Outline each blood parasite and name the species.
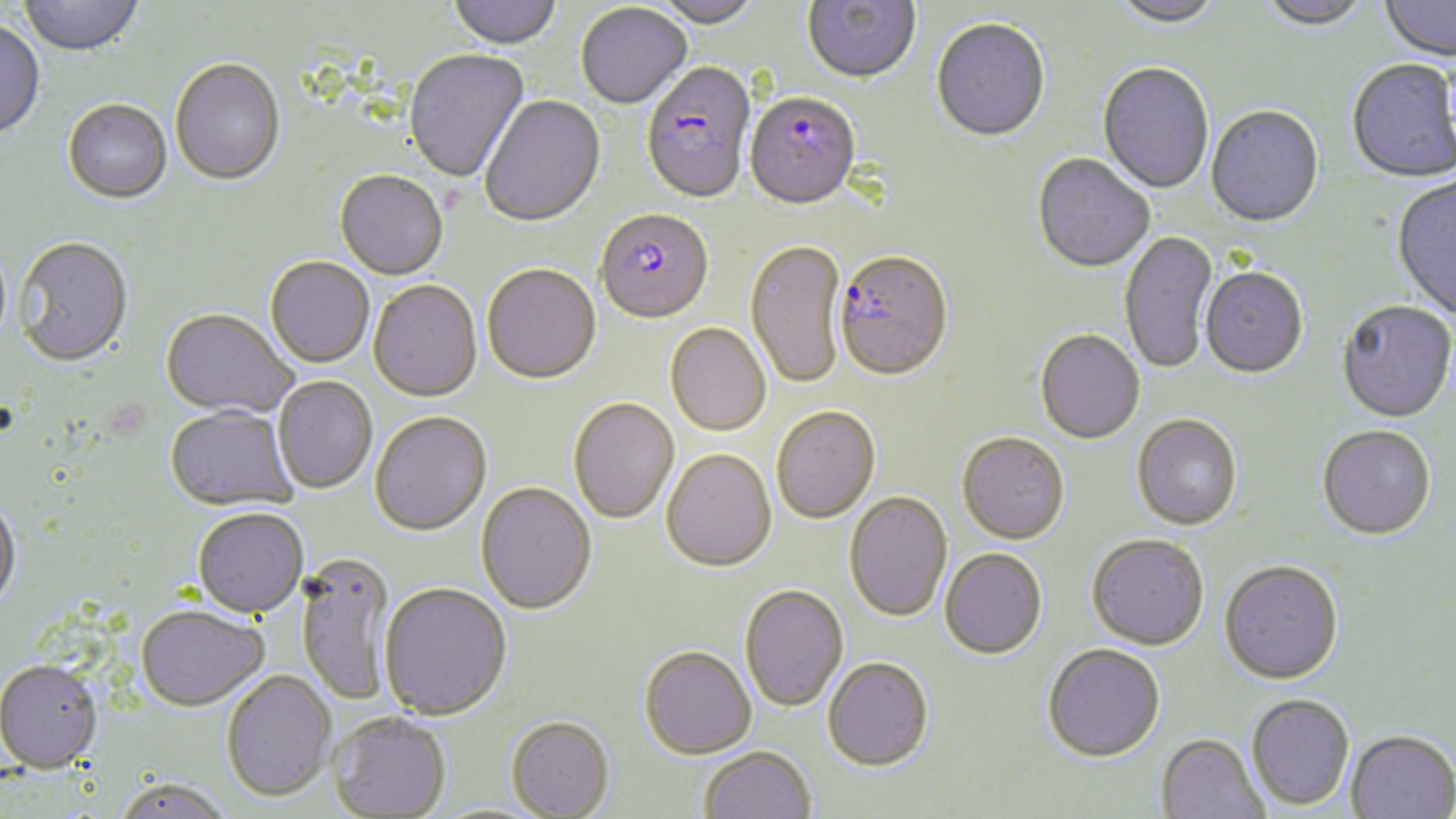
Approximate bounding boxes as named x1/y1/x2/y2 corners in pixels.
Plasmodium falciparum-infected red blood cells: (x1=641, y1=63, x2=756, y2=207), (x1=744, y1=90, x2=866, y2=212), (x1=595, y1=211, x2=714, y2=327), (x1=834, y1=253, x2=954, y2=384).
No Plasmodium ovale, Plasmodium malariae, Plasmodium vivax, Babesia divergens, or Trypanosoma brucei observed.

Uninfected red blood cell locations: (x1=18, y1=0, x2=145, y2=58), (x1=448, y1=0, x2=561, y2=51), (x1=650, y1=0, x2=763, y2=31), (x1=802, y1=0, x2=920, y2=86), (x1=1110, y1=0, x2=1223, y2=29), (x1=1257, y1=0, x2=1373, y2=33), (x1=1380, y1=1, x2=1455, y2=63), (x1=576, y1=4, x2=692, y2=111), (x1=931, y1=19, x2=1050, y2=144), (x1=0, y1=22, x2=45, y2=142), (x1=404, y1=50, x2=530, y2=184), (x1=170, y1=60, x2=285, y2=188), (x1=1347, y1=60, x2=1455, y2=184), (x1=1097, y1=63, x2=1213, y2=196), (x1=480, y1=96, x2=607, y2=230), (x1=62, y1=101, x2=172, y2=205), (x1=1206, y1=107, x2=1324, y2=230), (x1=1032, y1=155, x2=1154, y2=275), (x1=334, y1=172, x2=448, y2=282), (x1=1391, y1=177, x2=1456, y2=322), (x1=1118, y1=231, x2=1220, y2=376), (x1=13, y1=238, x2=134, y2=369), (x1=745, y1=241, x2=847, y2=392), (x1=265, y1=258, x2=374, y2=370), (x1=482, y1=266, x2=601, y2=386), (x1=1200, y1=269, x2=1308, y2=381), (x1=368, y1=281, x2=481, y2=403), (x1=1336, y1=301, x2=1456, y2=424), (x1=160, y1=310, x2=298, y2=419), (x1=665, y1=324, x2=771, y2=438), (x1=1035, y1=331, x2=1145, y2=446), (x1=273, y1=377, x2=377, y2=494), (x1=568, y1=399, x2=680, y2=525), (x1=165, y1=406, x2=298, y2=512), (x1=772, y1=408, x2=880, y2=526), (x1=370, y1=412, x2=493, y2=537), (x1=1132, y1=416, x2=1243, y2=532), (x1=1317, y1=425, x2=1436, y2=541), (x1=957, y1=434, x2=1069, y2=546), (x1=662, y1=450, x2=776, y2=574), (x1=475, y1=482, x2=597, y2=616), (x1=844, y1=492, x2=952, y2=623), (x1=0, y1=494, x2=23, y2=615), (x1=192, y1=507, x2=309, y2=618), (x1=1086, y1=535, x2=1209, y2=652), (x1=939, y1=550, x2=1047, y2=661), (x1=297, y1=553, x2=396, y2=707), (x1=1219, y1=561, x2=1344, y2=685), (x1=379, y1=584, x2=512, y2=721), (x1=740, y1=585, x2=848, y2=714), (x1=135, y1=604, x2=270, y2=711), (x1=1042, y1=644, x2=1166, y2=762), (x1=638, y1=646, x2=757, y2=760), (x1=822, y1=658, x2=934, y2=772), (x1=0, y1=659, x2=102, y2=773), (x1=221, y1=670, x2=336, y2=802), (x1=1246, y1=693, x2=1354, y2=810), (x1=328, y1=711, x2=451, y2=818), (x1=506, y1=715, x2=615, y2=818), (x1=1346, y1=729, x2=1456, y2=819), (x1=1156, y1=732, x2=1269, y2=819), (x1=699, y1=746, x2=816, y2=819), (x1=115, y1=777, x2=232, y2=819). Platelet locations: (x1=106, y1=395, x2=153, y2=444). Slide-level diagnosis: Plasmodium falciparum. Thin blood smear. Captured at 1000x magnification. Image is 1456×819 pixels. May-Grünwald-Giemsa-stained preparation. Light microscopy. One field of a larger specimen.